Assess for Plasmodium parasites.
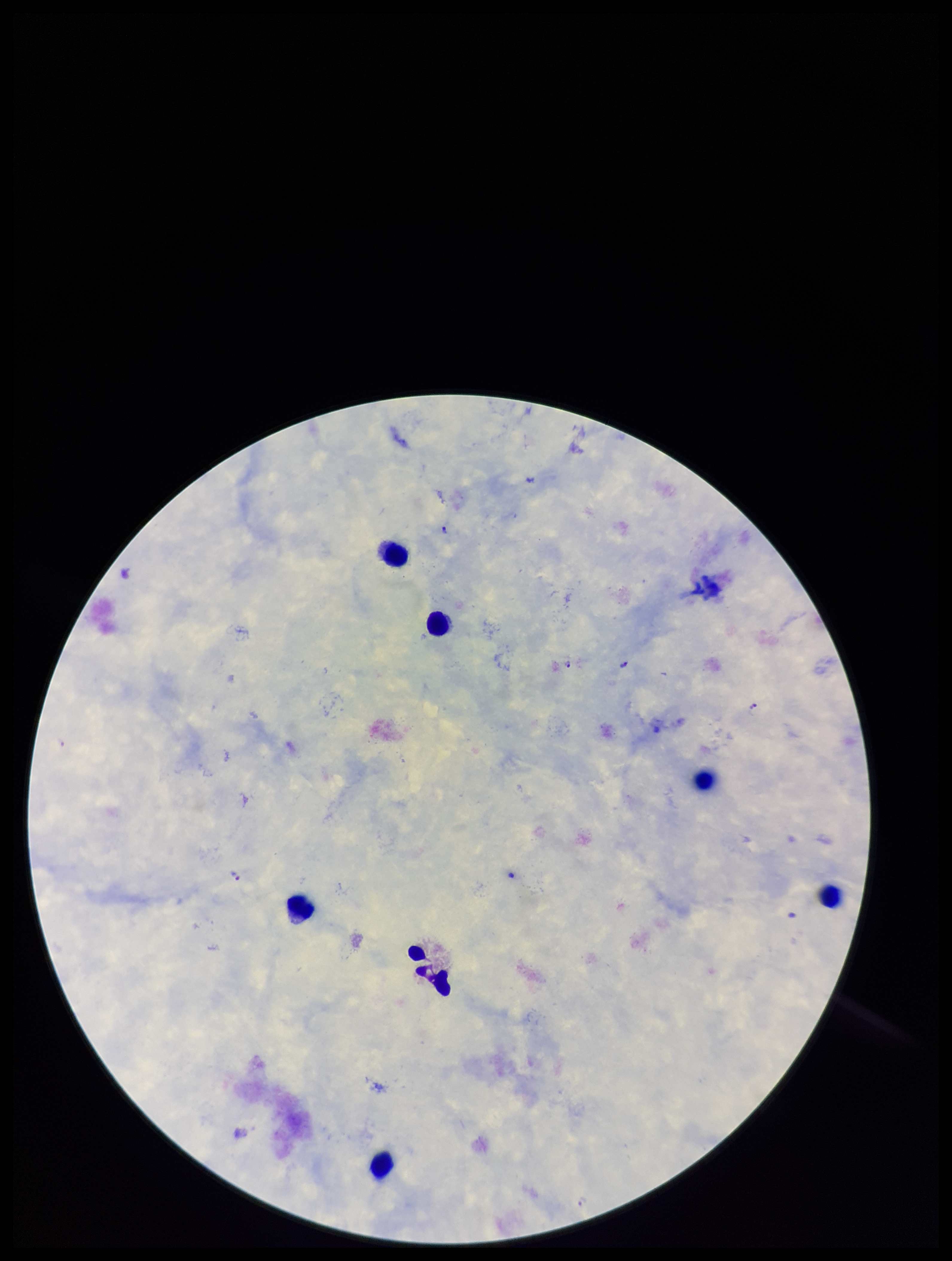
Seen.

Species reported for this patient: Plasmodium falciparum. Stained with Giemsa. Image is 952×1261 pixels. Patient malaria status: positive. Leukocyte count: 7. Single field of view. Smartphone photograph taken through the eyepiece of a microscope. Parasite count: 4. Preparation: thick blood smear.